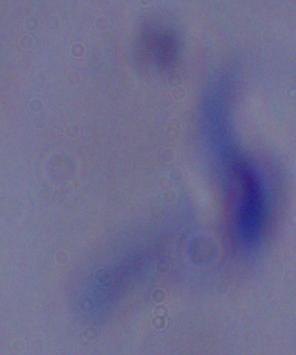
Summary:
  - Modality: photomicrograph
  - Identification: trypanosome
  - Magnification: 1000x